Report the malaria status of this cell.
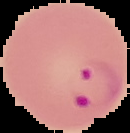
It is parasitized.

image size = 130×133 pixels
preparation = thin blood film
image type = segmented cell region with the area outside set to black